Describe the morphology of the red blood cells.
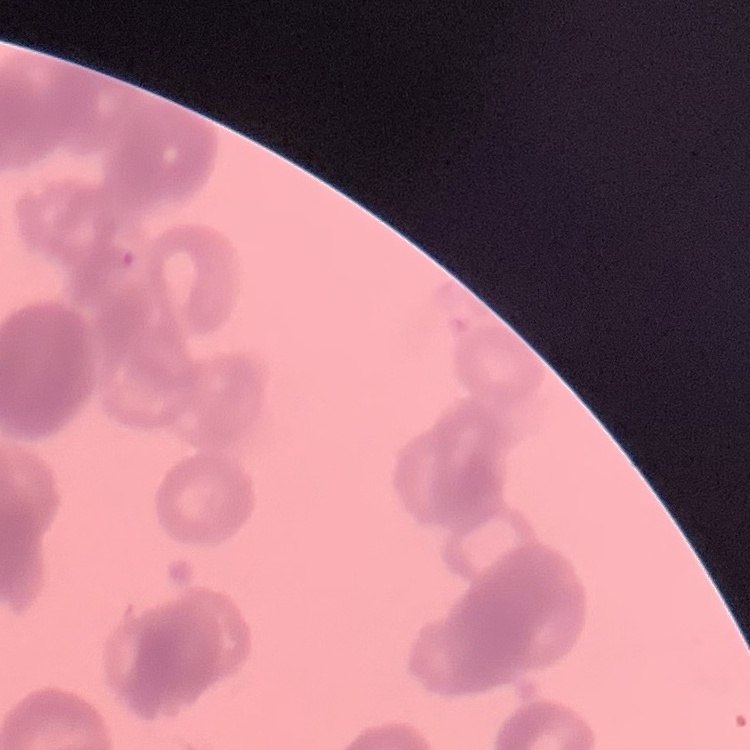
Rouleaux formation.

Square crop of a larger photomicrograph. Field's or Giemsa stain. Thin blood smear.